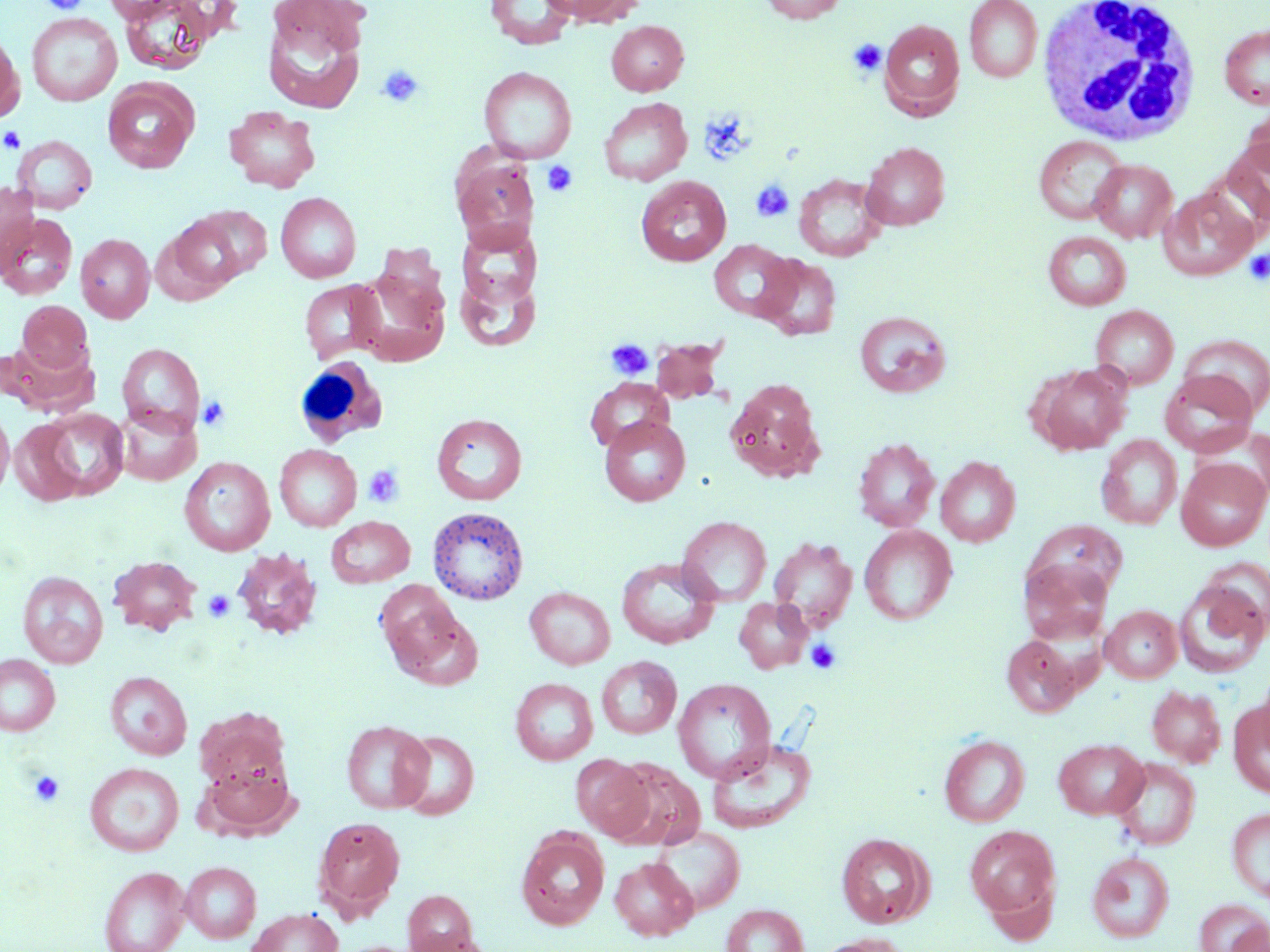
Approximate bounding boxes as (x1, y1, x2, y2) in pixels. White blood cell locations: (1035, 0, 1205, 146), (294, 357, 387, 447). Platelet locations: (39, 0, 91, 14), (848, 39, 886, 77), (377, 64, 425, 108), (1, 126, 25, 154), (542, 160, 578, 197), (752, 178, 795, 222), (1245, 249, 1270, 284), (605, 338, 654, 381), (197, 395, 231, 432), (362, 463, 405, 508), (203, 589, 236, 621), (806, 638, 842, 674), (29, 771, 64, 806). Uninfected red blood cell locations: (116, 0, 220, 74), (538, 0, 639, 26), (760, 0, 846, 23), (964, 0, 1043, 82), (262, 1, 371, 114), (485, 1, 578, 49), (27, 12, 122, 106), (879, 19, 965, 118), (607, 20, 688, 96), (1219, 24, 1270, 110), (0, 28, 24, 123), (479, 66, 577, 163), (102, 81, 198, 173), (598, 98, 692, 186), (1241, 102, 1270, 177), (224, 105, 321, 192), (13, 135, 98, 213), (1034, 135, 1128, 225), (1222, 136, 1270, 230), (861, 142, 950, 231), (451, 151, 539, 252), (1090, 159, 1177, 243), (793, 173, 888, 262), (636, 176, 731, 266), (0, 182, 39, 275), (1158, 188, 1256, 280), (275, 192, 361, 283), (196, 205, 273, 279), (0, 213, 78, 300), (162, 216, 245, 296), (455, 223, 541, 314), (1043, 231, 1132, 310), (76, 233, 155, 323), (709, 239, 796, 322), (757, 255, 841, 340), (353, 261, 452, 366), (454, 267, 541, 353), (299, 280, 386, 364), (17, 300, 93, 376), (1091, 305, 1178, 389), (854, 310, 951, 397), (1178, 334, 1270, 419), (651, 338, 728, 404), (3, 339, 98, 419), (117, 343, 205, 435), (1032, 364, 1129, 455), (1160, 371, 1258, 458), (585, 378, 673, 452), (725, 379, 825, 482), (113, 403, 200, 486), (0, 406, 14, 501), (27, 407, 129, 503), (431, 413, 528, 505), (599, 415, 691, 506), (7, 418, 86, 506), (1247, 426, 1270, 503), (1097, 435, 1182, 530), (853, 437, 940, 532), (274, 444, 362, 532), (1098, 444, 1270, 538), (181, 451, 361, 541), (936, 456, 1020, 547), (179, 457, 275, 556), (1176, 458, 1269, 551), (426, 506, 529, 606), (326, 516, 415, 587), (677, 516, 772, 606), (1025, 520, 1128, 604), (859, 525, 957, 625), (768, 537, 858, 634), (231, 549, 323, 640), (109, 554, 201, 635), (617, 558, 719, 649), (1201, 558, 1270, 637), (1019, 559, 1113, 644), (18, 571, 109, 668), (1174, 579, 1268, 678), (375, 581, 465, 672), (524, 587, 615, 669), (734, 598, 813, 673), (1101, 605, 1182, 683), (388, 606, 483, 692), (1002, 634, 1080, 717), (0, 654, 60, 736), (597, 656, 681, 739), (1257, 664, 1270, 757), (105, 671, 192, 760), (511, 677, 598, 765), (673, 678, 776, 783), (1148, 685, 1226, 767), (1229, 699, 1270, 799), (194, 710, 292, 798), (342, 720, 433, 813), (393, 730, 479, 820), (939, 734, 1030, 827), (708, 737, 817, 833), (1054, 738, 1149, 819), (571, 754, 654, 840), (1111, 757, 1201, 850), (610, 760, 706, 851), (200, 761, 298, 839), (85, 762, 184, 856), (1227, 807, 1270, 901), (313, 816, 405, 919), (964, 825, 1061, 921), (652, 826, 745, 915), (516, 830, 609, 929), (836, 833, 932, 928), (1087, 851, 1175, 943), (610, 857, 697, 940), (180, 861, 261, 943), (99, 865, 190, 952), (403, 889, 478, 951), (1194, 899, 1269, 952), (720, 904, 810, 952), (247, 907, 343, 952), (406, 933, 497, 952), (815, 933, 909, 952). Slide-level diagnosis: negative for blood parasites. Thin blood smear. Single field of view. Optical microscopy. Image is 1270×952 pixels. 1000x magnification. May-Grünwald-Giemsa stain.